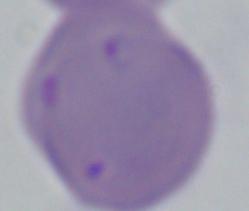

Micrograph. 1000x magnification. A Babesia parasite is shown.